Report the malaria status of this cell.
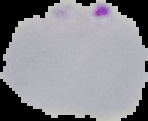

Parasitized.

image_size: 148×121 pixels
image_type: segmented cell region on a black background
preparation: thin blood smear